Give the position of every Plasmodium parasite visible.
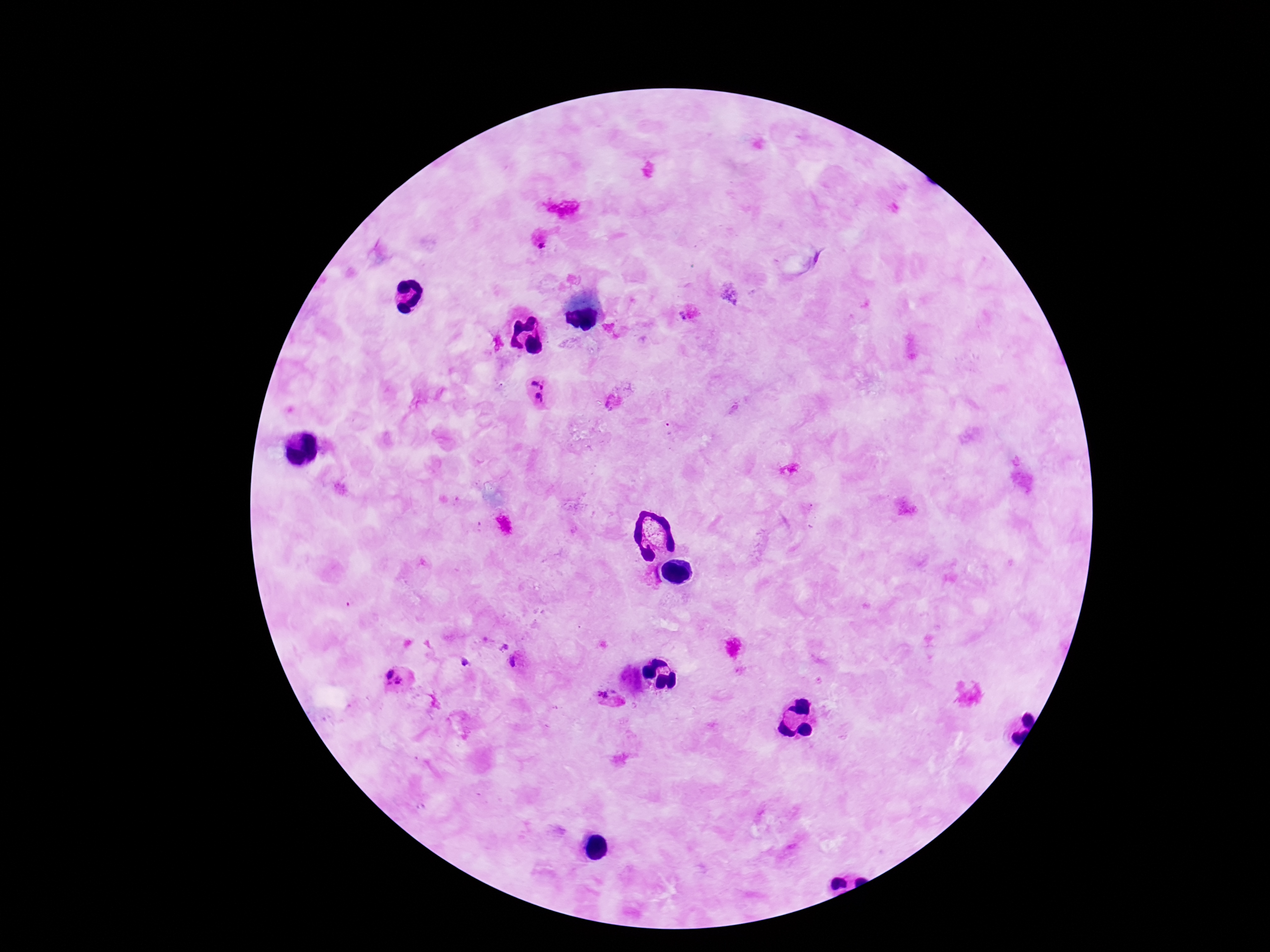

Approximate centers as {x, y} in pixels.
Plasmodium parasites: {539, 243}, {685, 315}, {539, 379}, {539, 400}, {612, 406}, {503, 648}, {515, 661}, {465, 662}, {388, 672}, {397, 684}, {607, 697}.

Summary:
  - Preparation: thick blood film
  - Stain: Giemsa
  - Patient malaria status: infected
  - Field of view: single
  - Capture: smartphone camera through the microscope eyepiece
  - Image size: 1270×952 pixels
  - Magnification: 100x